Comment on the morphology of the erythrocytes.
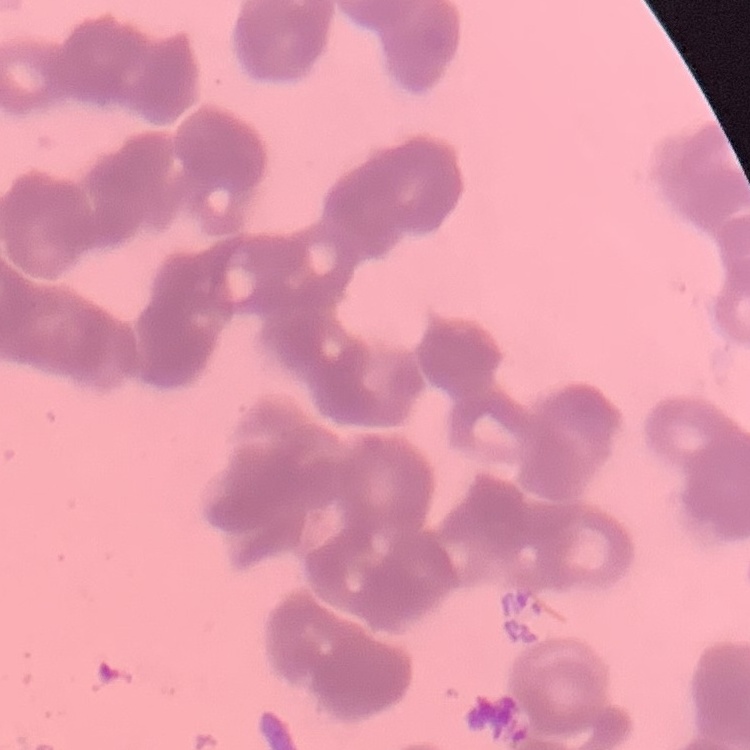

They show rouleaux formation.

preparation: thin blood smear
image_type: square crop of a larger photomicrograph
stain: Field's or Giemsa